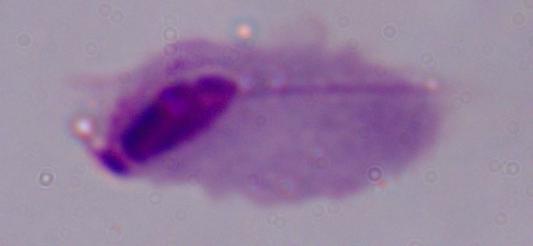
Summary:
  - Magnification: 1000x
  - Modality: micrograph
  - Identification: trichomonad